Identify the preparation type.
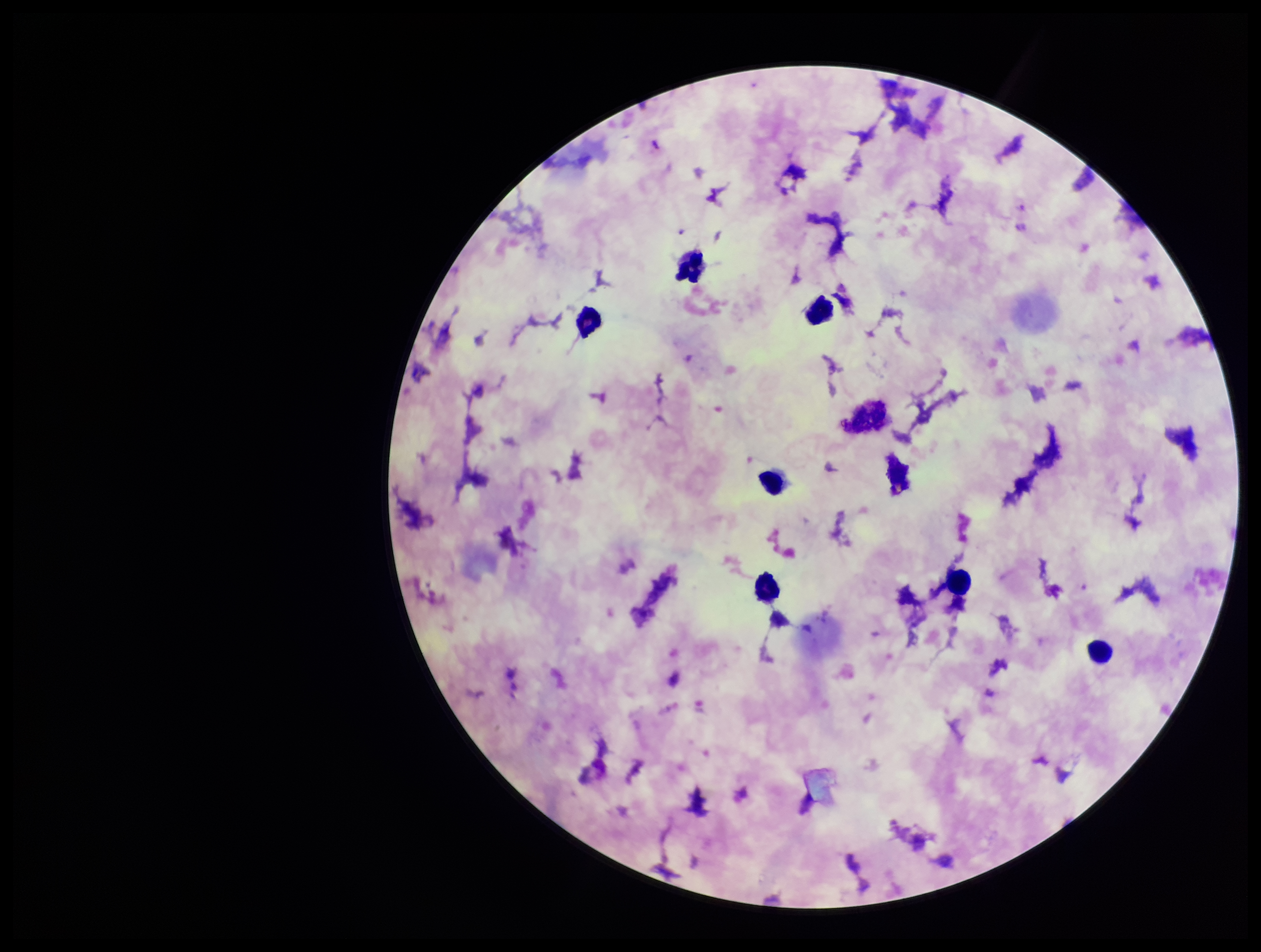
Thick.

Summary:
  - Species reported for this patient: Plasmodium falciparum
  - Patient malaria status: infected
  - Capture: smartphone photograph through the microscope eyepiece
  - Parasite count: 1
  - Image size: 1261×952 pixels
  - Plasmodium parasites: seen
  - Field of view: one from this slide
  - Stain: Giemsa
  - Leukocyte count: 7